Comment on the morphology of the red blood cells.
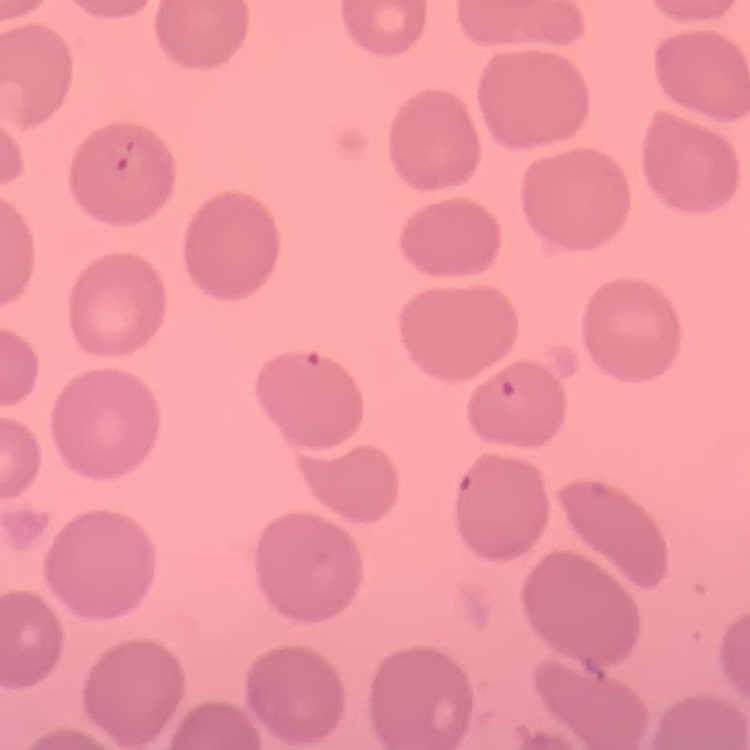

No rouleaux formation.

preparation = thin blood smear
image type = one tile cut from a larger photomicrograph
stain = Field's or Giemsa